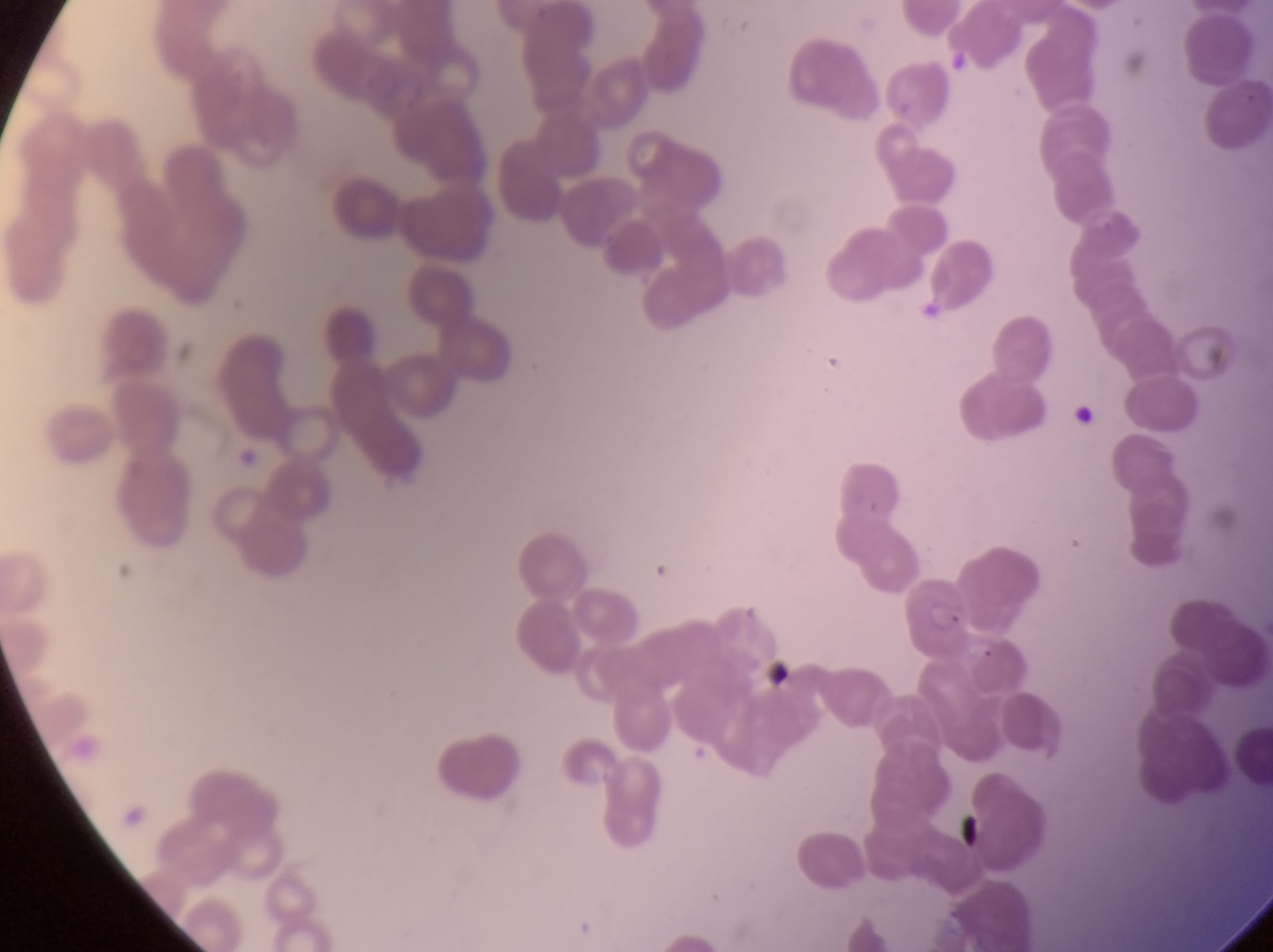
{
  "preparation": "thin blood smear",
  "field_of_view": "single",
  "capture": "smartphone photograph through the eyepiece of an Olympus CX-23 microscope",
  "image_size": "1273×952 pixels",
  "country": "Uganda",
  "magnification": "1000x",
  "artifact_platelet_like_body_stain_precipitate_or_debris_locations": "approximate bounding boxes as left top right bottom in pixels: 1071 402 1098 432; 759 654 801 699; 954 809 996 861",
  "parasitised_red_blood_cell_locations": "approximate bounding boxes as left top right bottom in pixels: 908 577 973 667"
}